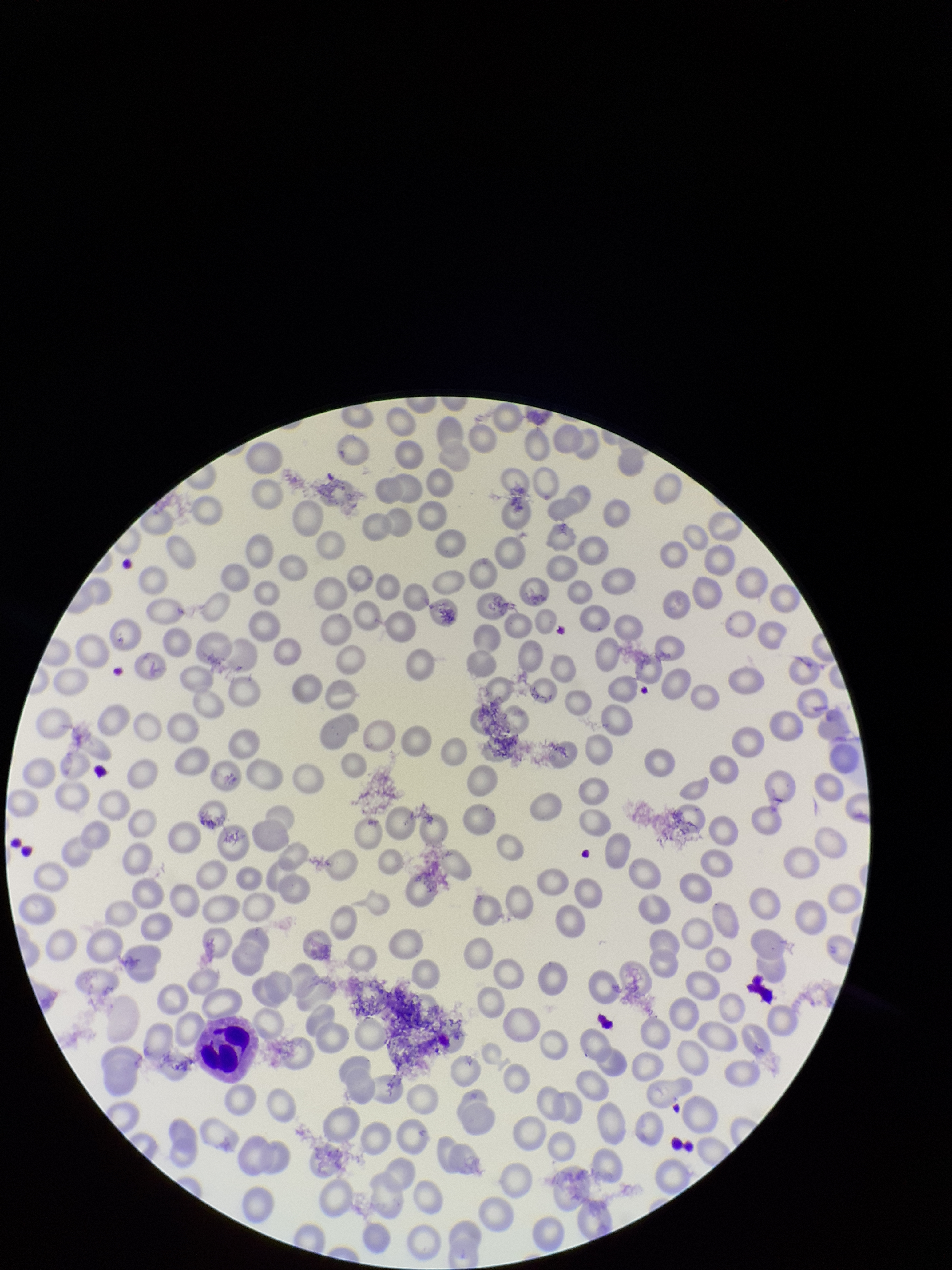
Giemsa stain. Preparation: thin blood smear. Photographed through the microscope eyepiece with a smartphone camera. Single field of view. Image is 952×1270 pixels. Patient malaria status: negative. Red blood cell count: 233. Parasitized red blood cell count: 0. Parasitized red blood cells: none detected.